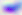

Photomicrograph. Toxoplasma gondii is seen. 400x magnification.